Report the malaria status of this cell.
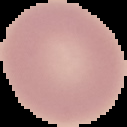
Uninfected.

image_type: cell region segmented out of the field of view; surrounding area masked to black
preparation: thin blood smear
image_size: 127×127 pixels